Give the preparation type.
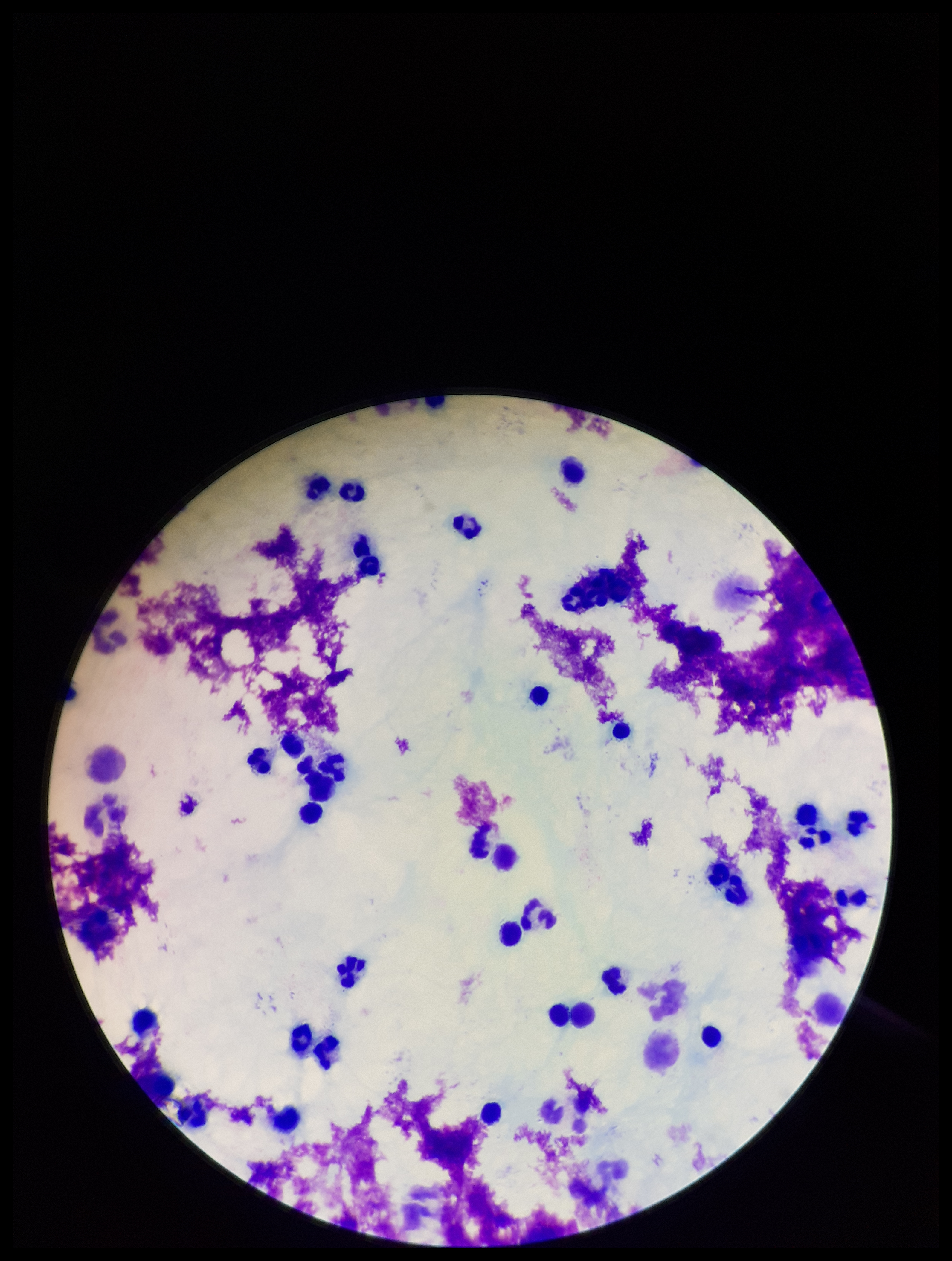
A thick smear.

Patient malaria status: negative. Single field of view. Image is 952×1261 pixels. Plasmodium parasites: none seen. Smartphone photograph taken through the eyepiece of a microscope. Parasite count: 0. Giemsa stain. Leukocyte count: 32.